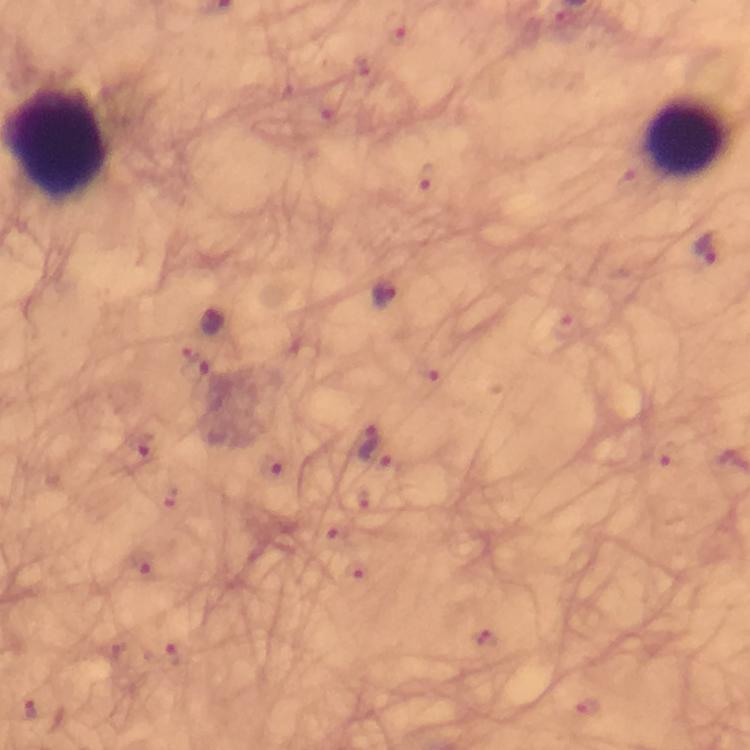

Approximate centers as (x, y) in pixels.
Summary:
  - Leukocyte locations: (686, 138)
  - Malaria parasite locations: (424, 176), (706, 248), (385, 293), (212, 321), (197, 365), (373, 446), (146, 447), (668, 453), (271, 465), (333, 538), (141, 563), (170, 656), (30, 708)
  - Stain: Giemsa
  - Cropped from: a single field of view
  - Context: from a diagnostic examination for malaria
  - Capture: smartphone photograph through a microscope
  - Immersion oil: used
  - Magnification: 100x
  - Image size: 750×750 pixels
  - Preparation: thick smear